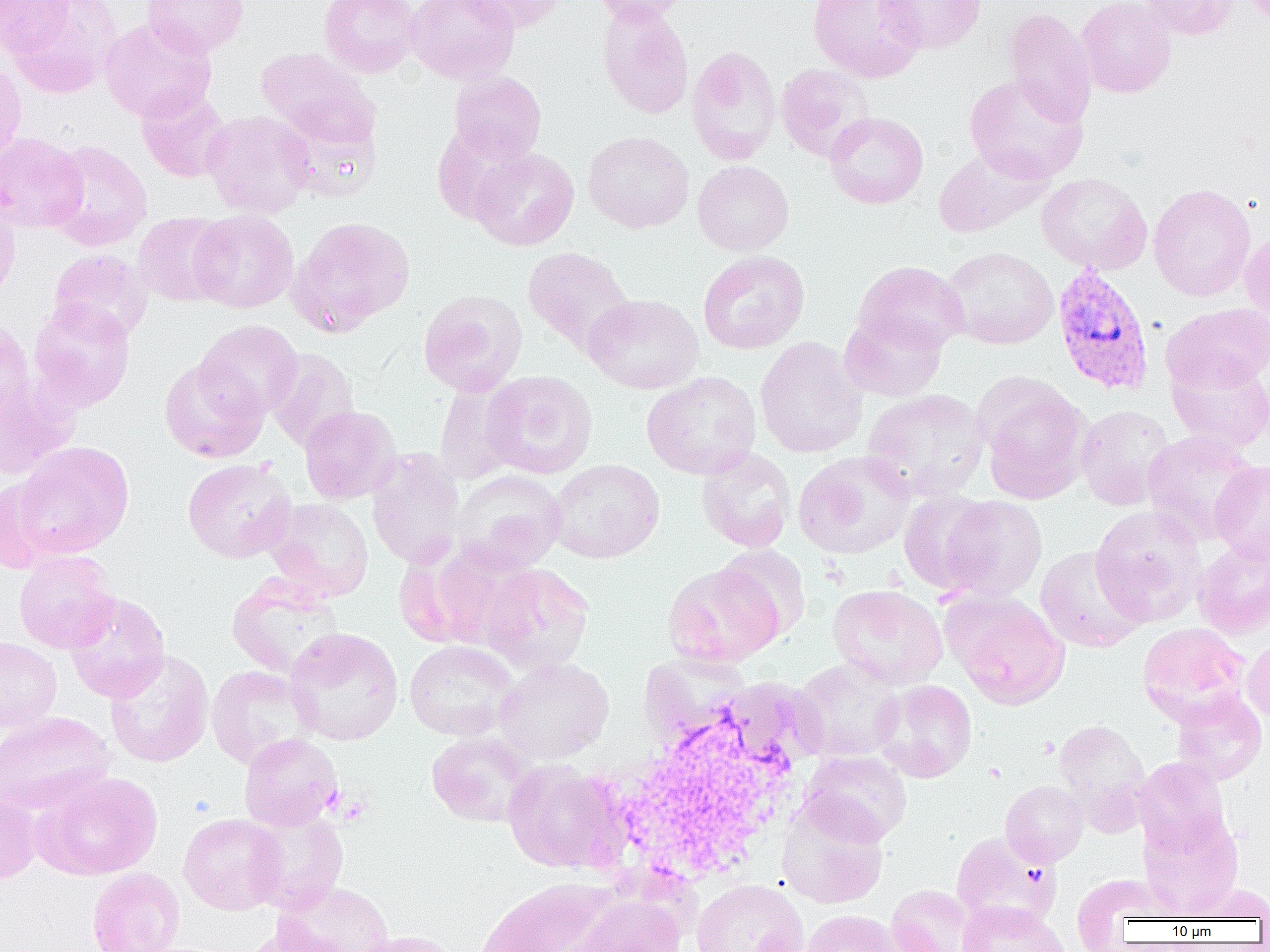

slide-level diagnosis = Plasmodium vivax
preparation = thin blood film
Plasmodium vivax-infected red blood cell locations = approximate bounding boxes as (x1, y1, x2, y2) in pixels: (1052, 265, 1155, 395)
modality = light microscopy
image size = 1270×952 pixels
uninfected red blood cell locations = approximate bounding boxes as (x1, y1, x2, y2) in pixels: (0, 0, 72, 59), (6, 0, 122, 98), (142, 0, 249, 58), (319, 0, 423, 78), (407, 0, 520, 85), (463, 0, 570, 32), (590, 0, 695, 24), (807, 0, 926, 82), (877, 0, 987, 54), (1075, 0, 1176, 98), (1137, 0, 1239, 40), (596, 3, 694, 120), (1003, 8, 1096, 125), (99, 18, 217, 122), (686, 45, 782, 165), (254, 47, 378, 149), (0, 57, 26, 166), (776, 64, 874, 162), (449, 71, 547, 164), (964, 73, 1089, 184), (135, 87, 233, 183), (275, 108, 382, 202), (201, 110, 315, 218), (824, 112, 928, 209), (432, 123, 531, 225), (583, 130, 694, 233), (0, 132, 87, 233), (44, 140, 152, 251), (933, 146, 1053, 238), (469, 147, 580, 251), (692, 160, 794, 256), (1036, 172, 1152, 275), (1148, 183, 1256, 301), (0, 191, 22, 303), (189, 210, 299, 313), (132, 212, 232, 307), (288, 215, 416, 336), (1241, 229, 1270, 325), (942, 246, 1058, 350), (522, 247, 635, 354), (47, 249, 152, 344), (698, 250, 809, 354), (854, 261, 969, 354), (418, 288, 527, 396), (583, 293, 704, 394), (28, 299, 135, 412), (1163, 302, 1270, 392), (839, 310, 948, 402), (0, 316, 34, 424), (196, 319, 303, 420), (755, 336, 868, 458), (266, 347, 360, 451), (1166, 355, 1270, 452), (159, 357, 269, 463), (481, 370, 598, 479), (642, 371, 762, 480), (977, 374, 1092, 504), (0, 375, 78, 480), (434, 379, 522, 485), (861, 388, 990, 502), (1076, 405, 1175, 511), (299, 406, 399, 504), (1141, 430, 1262, 544), (13, 441, 135, 559), (696, 447, 796, 552), (366, 450, 465, 570), (794, 451, 916, 559), (182, 458, 297, 563), (548, 459, 664, 563), (1210, 460, 1270, 564), (452, 470, 566, 572), (1, 476, 64, 572), (898, 490, 996, 595), (937, 495, 1047, 603), (265, 498, 374, 601), (1090, 504, 1207, 626), (1194, 537, 1270, 639), (423, 543, 541, 650), (712, 544, 811, 642), (1035, 545, 1150, 654), (14, 550, 119, 653), (480, 563, 595, 674), (662, 564, 782, 667), (226, 575, 346, 679), (827, 584, 948, 690), (64, 591, 170, 704), (946, 592, 1070, 710), (1137, 623, 1250, 724), (284, 627, 404, 746), (0, 637, 62, 731), (1243, 637, 1270, 724), (404, 640, 519, 740), (104, 649, 214, 768), (639, 652, 750, 746), (494, 656, 614, 764), (791, 657, 905, 762), (206, 665, 320, 770), (874, 680, 977, 782), (1171, 690, 1267, 785), (0, 711, 115, 815), (1053, 718, 1151, 825), (426, 731, 538, 828), (238, 733, 342, 831), (798, 750, 912, 846), (1134, 756, 1230, 855), (503, 760, 626, 874), (34, 771, 162, 879), (1000, 780, 1088, 867), (0, 791, 43, 886), (777, 800, 888, 909), (244, 808, 349, 914), (1139, 810, 1244, 919), (178, 813, 286, 915), (950, 832, 1059, 929), (86, 866, 185, 952), (1070, 872, 1175, 947), (477, 877, 620, 952), (692, 879, 808, 952), (273, 880, 393, 952), (1184, 882, 1270, 921), (887, 884, 975, 952), (570, 896, 686, 952), (957, 901, 1068, 952), (800, 909, 906, 952), (236, 925, 352, 952), (350, 930, 460, 952)
field of view = single
magnification = 1000x
platelet locations = approximate bounding boxes as (x1, y1, x2, y2) in pixels: (335, 795, 371, 826)